Locate every blood parasite and identify its species.
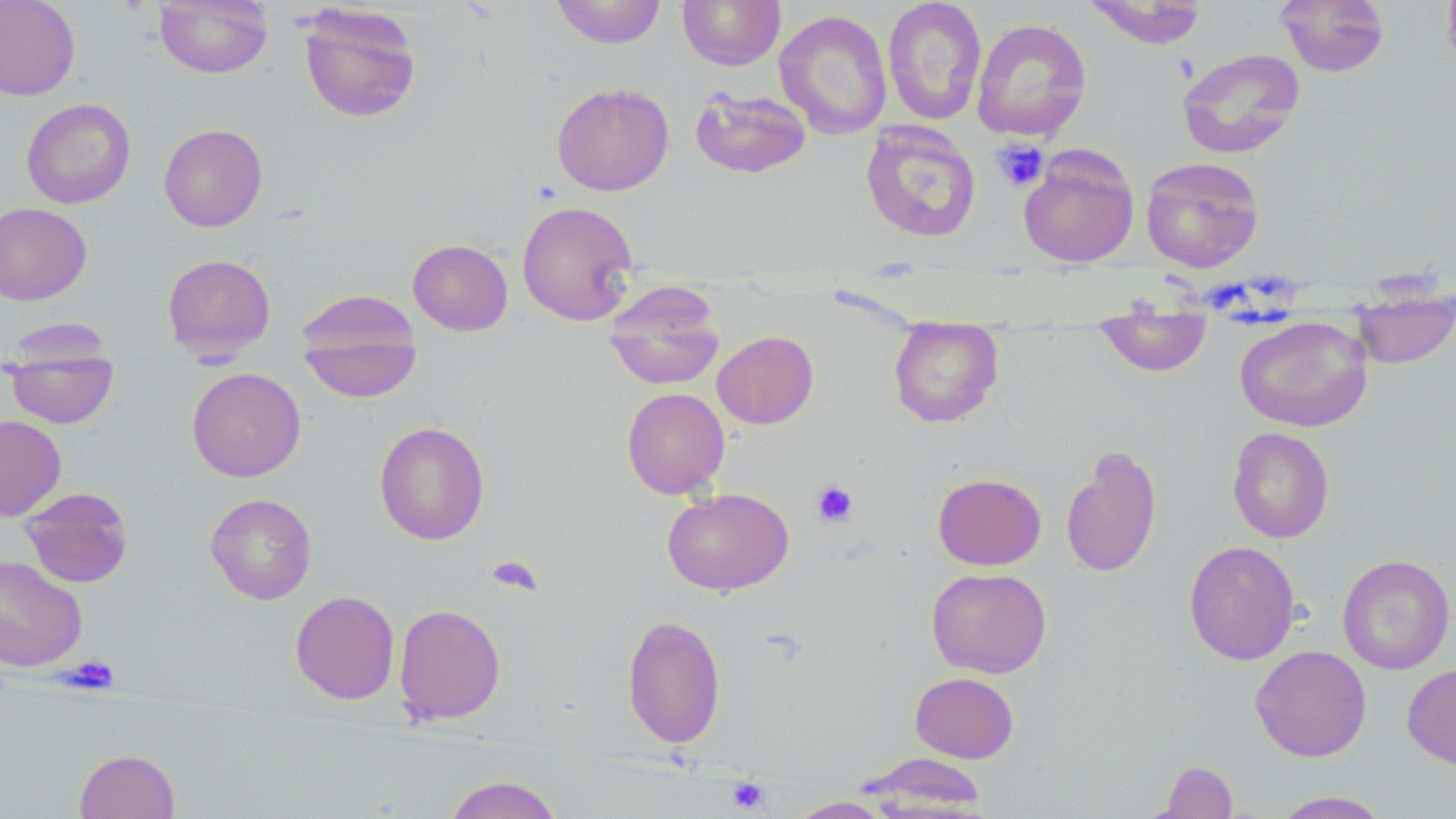

No blood parasites seen.

Summary:
  - Coordinate format: approximate bounding boxes as named x1/y1/x2/y2 corners in pixels
  - Platelet locations: (x1=991, y1=139, x2=1049, y2=192), (x1=811, y1=480, x2=858, y2=527), (x1=487, y1=554, x2=544, y2=597), (x1=66, y1=657, x2=120, y2=693), (x1=727, y1=776, x2=771, y2=813)
  - Uninfected red blood cell locations: (x1=0, y1=0, x2=81, y2=100), (x1=154, y1=0, x2=272, y2=78), (x1=551, y1=0, x2=667, y2=49), (x1=677, y1=0, x2=786, y2=70), (x1=882, y1=0, x2=987, y2=126), (x1=1083, y1=0, x2=1208, y2=49), (x1=1276, y1=0, x2=1390, y2=76), (x1=1441, y1=0, x2=1456, y2=77), (x1=297, y1=3, x2=422, y2=124), (x1=774, y1=9, x2=892, y2=139), (x1=971, y1=18, x2=1092, y2=142), (x1=1176, y1=47, x2=1305, y2=159), (x1=552, y1=82, x2=674, y2=196), (x1=690, y1=87, x2=811, y2=179), (x1=21, y1=98, x2=136, y2=209), (x1=860, y1=121, x2=981, y2=243), (x1=159, y1=123, x2=268, y2=232), (x1=1018, y1=147, x2=1139, y2=268), (x1=1140, y1=156, x2=1265, y2=273), (x1=516, y1=201, x2=638, y2=326), (x1=0, y1=203, x2=92, y2=305), (x1=408, y1=239, x2=513, y2=336), (x1=161, y1=253, x2=276, y2=358), (x1=604, y1=282, x2=725, y2=390), (x1=1351, y1=286, x2=1455, y2=369), (x1=296, y1=300, x2=422, y2=402), (x1=1094, y1=313, x2=1212, y2=377), (x1=1234, y1=315, x2=1373, y2=432), (x1=889, y1=319, x2=1003, y2=428), (x1=712, y1=330, x2=819, y2=430), (x1=4, y1=344, x2=119, y2=428), (x1=186, y1=367, x2=306, y2=482), (x1=621, y1=387, x2=730, y2=498), (x1=0, y1=415, x2=66, y2=520), (x1=373, y1=421, x2=490, y2=545), (x1=1227, y1=427, x2=1335, y2=543), (x1=1060, y1=445, x2=1163, y2=579), (x1=933, y1=473, x2=1046, y2=570), (x1=20, y1=487, x2=134, y2=588), (x1=662, y1=488, x2=793, y2=596), (x1=205, y1=492, x2=318, y2=605), (x1=1183, y1=540, x2=1300, y2=665), (x1=1337, y1=554, x2=1455, y2=674), (x1=0, y1=555, x2=87, y2=671), (x1=926, y1=567, x2=1052, y2=678), (x1=290, y1=589, x2=400, y2=705), (x1=393, y1=603, x2=506, y2=725), (x1=622, y1=614, x2=726, y2=748), (x1=1250, y1=644, x2=1372, y2=762), (x1=1402, y1=662, x2=1456, y2=769), (x1=909, y1=671, x2=1019, y2=763), (x1=74, y1=749, x2=180, y2=819), (x1=858, y1=753, x2=988, y2=813), (x1=1156, y1=760, x2=1239, y2=818), (x1=443, y1=775, x2=564, y2=819), (x1=1271, y1=790, x2=1391, y2=818), (x1=787, y1=796, x2=893, y2=818)
  - Slide-level diagnosis: no evidence of blood parasites
  - Field of view: single
  - Stain: May-Grünwald-Giemsa
  - Preparation: thin blood film
  - Magnification: 1000x
  - Modality: optical microscopy
  - Image size: 1456×819 pixels